Look for parasitized red blood cells.
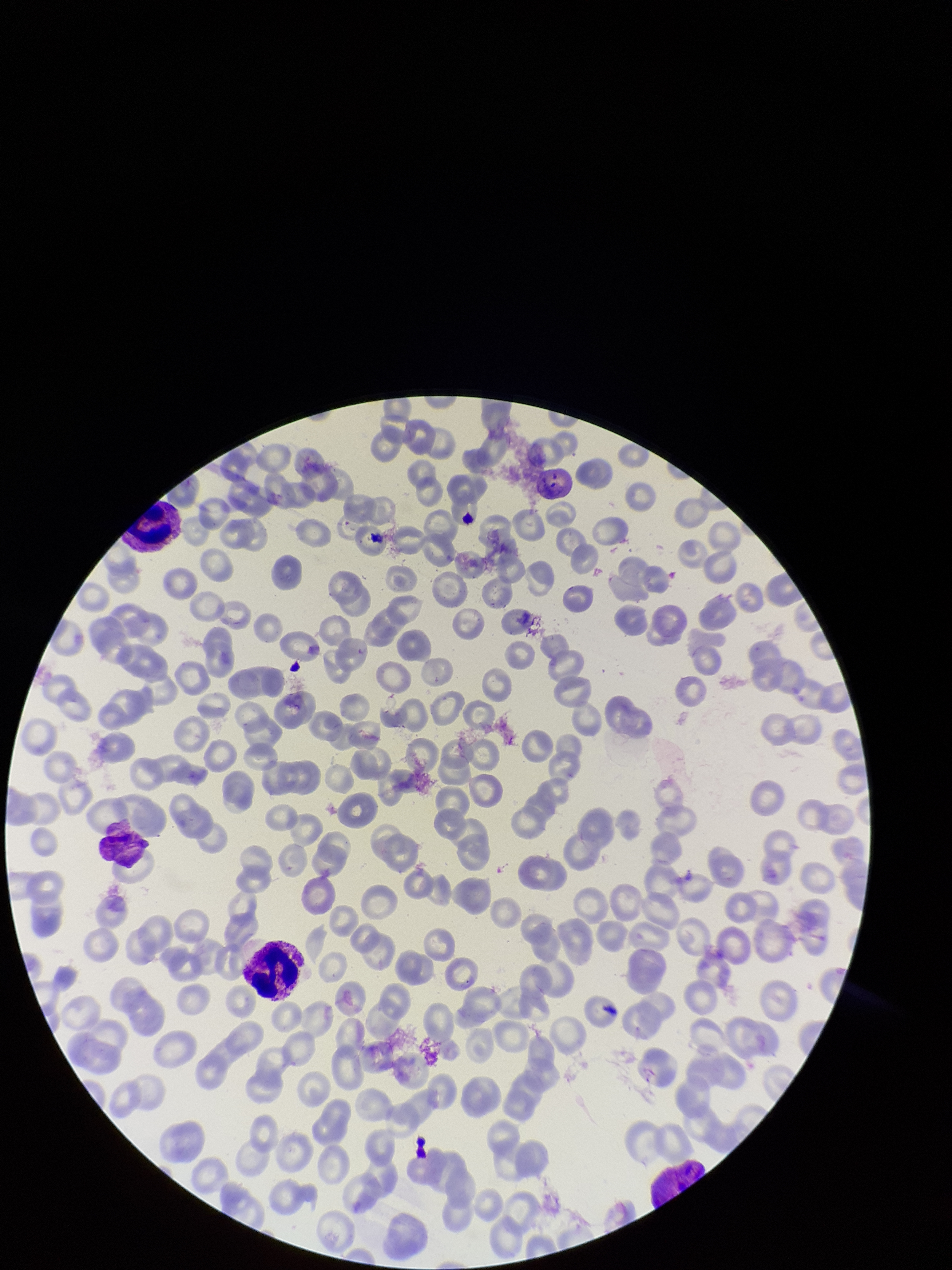
Detected.

patient malaria status = positive
image size = 952×1270 pixels
red blood cell count = 197
species reported for this patient = Plasmodium vivax
preparation = thin smear
field of view = single
capture = smartphone photograph through the microscope eyepiece
stain = Giemsa
parasitized red blood cell count = 1